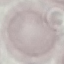

Result: no malaria parasites detected. Acquired by smartphone through the microscope eyepiece. Automatically extracted cell patch, resized to 64 × 64 pixels. Thin blood film. Giemsa-stained preparation.